Report the malaria status of this cell.
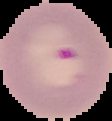
Parasitized.

image type = segmented cell region with the area outside set to black
image size = 112×121 pixels
preparation = thin blood smear